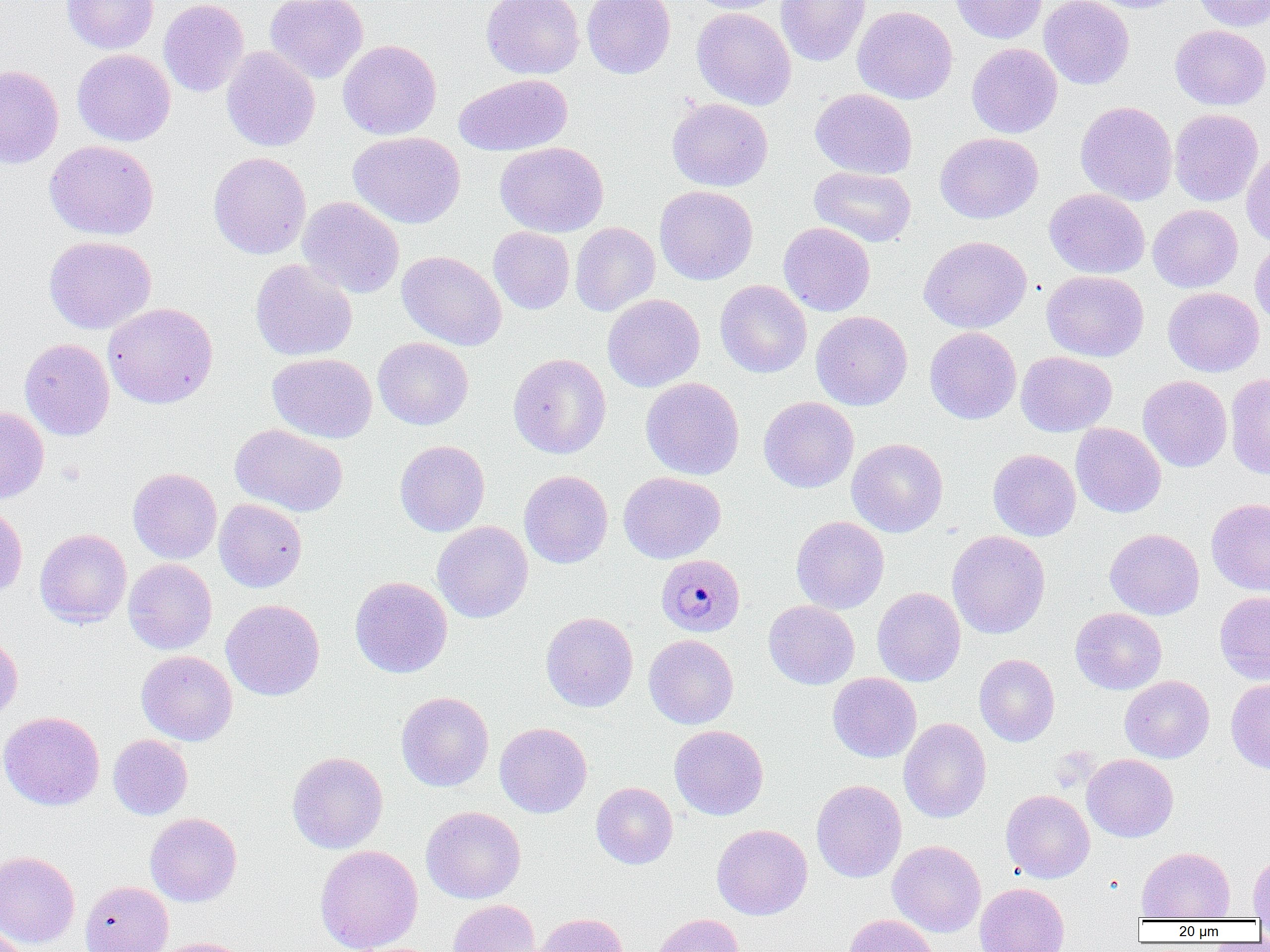
Summary:
  - Coordinate format: approximate bounding boxes as named x1/y1/x2/y2 corners in pixels
  - Plasmodium malariae-infected red blood cell locations: (x1=656, y1=553, x2=745, y2=637)
  - Uninfected red blood cell locations: (x1=61, y1=0, x2=159, y2=54), (x1=159, y1=0, x2=249, y2=97), (x1=265, y1=0, x2=368, y2=83), (x1=482, y1=0, x2=584, y2=79), (x1=582, y1=0, x2=676, y2=79), (x1=685, y1=0, x2=787, y2=14), (x1=776, y1=0, x2=871, y2=66), (x1=950, y1=0, x2=1047, y2=44), (x1=1039, y1=0, x2=1134, y2=89), (x1=1084, y1=0, x2=1187, y2=13), (x1=1191, y1=0, x2=1270, y2=32), (x1=852, y1=5, x2=958, y2=104), (x1=691, y1=7, x2=796, y2=110), (x1=1170, y1=25, x2=1270, y2=110), (x1=338, y1=39, x2=442, y2=140), (x1=966, y1=43, x2=1062, y2=138), (x1=221, y1=46, x2=320, y2=152), (x1=72, y1=49, x2=176, y2=147), (x1=0, y1=64, x2=64, y2=169), (x1=454, y1=73, x2=573, y2=156), (x1=810, y1=88, x2=918, y2=179), (x1=667, y1=97, x2=773, y2=191), (x1=1075, y1=101, x2=1177, y2=205), (x1=1169, y1=108, x2=1264, y2=206), (x1=348, y1=131, x2=466, y2=229), (x1=934, y1=132, x2=1043, y2=223), (x1=45, y1=140, x2=159, y2=240), (x1=496, y1=142, x2=609, y2=237), (x1=1241, y1=146, x2=1270, y2=246), (x1=208, y1=152, x2=312, y2=260), (x1=809, y1=165, x2=917, y2=247), (x1=654, y1=185, x2=758, y2=285), (x1=1044, y1=188, x2=1150, y2=278), (x1=297, y1=197, x2=405, y2=298), (x1=1148, y1=204, x2=1243, y2=293), (x1=570, y1=222, x2=660, y2=316), (x1=778, y1=222, x2=876, y2=316), (x1=488, y1=227, x2=575, y2=314), (x1=44, y1=235, x2=156, y2=334), (x1=918, y1=235, x2=1032, y2=333), (x1=1250, y1=240, x2=1270, y2=327), (x1=397, y1=250, x2=506, y2=350), (x1=250, y1=258, x2=358, y2=362), (x1=1042, y1=270, x2=1148, y2=361), (x1=715, y1=280, x2=812, y2=378), (x1=1163, y1=287, x2=1264, y2=377), (x1=602, y1=293, x2=705, y2=392), (x1=103, y1=302, x2=218, y2=409), (x1=811, y1=311, x2=912, y2=410), (x1=924, y1=326, x2=1022, y2=424), (x1=373, y1=337, x2=474, y2=430), (x1=19, y1=338, x2=115, y2=440), (x1=1016, y1=351, x2=1117, y2=436), (x1=267, y1=353, x2=377, y2=443), (x1=508, y1=353, x2=611, y2=458), (x1=1225, y1=373, x2=1270, y2=479), (x1=1138, y1=375, x2=1232, y2=472), (x1=640, y1=377, x2=744, y2=479), (x1=758, y1=396, x2=859, y2=493), (x1=0, y1=406, x2=49, y2=504), (x1=230, y1=423, x2=349, y2=517), (x1=1071, y1=423, x2=1166, y2=518), (x1=847, y1=438, x2=948, y2=537), (x1=395, y1=440, x2=490, y2=536), (x1=988, y1=449, x2=1081, y2=541), (x1=128, y1=468, x2=222, y2=564), (x1=519, y1=469, x2=613, y2=569), (x1=618, y1=471, x2=726, y2=563), (x1=214, y1=498, x2=307, y2=592), (x1=1206, y1=499, x2=1270, y2=596), (x1=0, y1=504, x2=27, y2=601), (x1=791, y1=516, x2=889, y2=614), (x1=432, y1=521, x2=533, y2=623), (x1=35, y1=528, x2=132, y2=628), (x1=1104, y1=528, x2=1204, y2=620), (x1=946, y1=531, x2=1050, y2=639), (x1=123, y1=559, x2=217, y2=654), (x1=350, y1=576, x2=453, y2=678), (x1=872, y1=587, x2=966, y2=686), (x1=1214, y1=591, x2=1270, y2=685), (x1=221, y1=599, x2=325, y2=701), (x1=763, y1=600, x2=860, y2=689), (x1=1070, y1=607, x2=1167, y2=694), (x1=540, y1=611, x2=638, y2=712), (x1=0, y1=633, x2=22, y2=726), (x1=644, y1=634, x2=739, y2=729), (x1=136, y1=650, x2=237, y2=745), (x1=974, y1=654, x2=1060, y2=746), (x1=827, y1=672, x2=921, y2=762), (x1=1119, y1=675, x2=1214, y2=763), (x1=1226, y1=678, x2=1270, y2=774), (x1=395, y1=691, x2=494, y2=791), (x1=0, y1=711, x2=104, y2=810), (x1=898, y1=718, x2=992, y2=823), (x1=495, y1=722, x2=592, y2=818), (x1=669, y1=725, x2=769, y2=820), (x1=107, y1=734, x2=193, y2=819), (x1=287, y1=751, x2=388, y2=853), (x1=1082, y1=754, x2=1178, y2=842), (x1=811, y1=779, x2=906, y2=883), (x1=591, y1=782, x2=678, y2=869), (x1=1001, y1=789, x2=1095, y2=883), (x1=421, y1=806, x2=526, y2=903), (x1=145, y1=813, x2=242, y2=906), (x1=712, y1=824, x2=812, y2=920), (x1=887, y1=840, x2=986, y2=937), (x1=314, y1=844, x2=423, y2=952), (x1=1137, y1=847, x2=1235, y2=920), (x1=0, y1=851, x2=80, y2=949), (x1=1248, y1=852, x2=1270, y2=919), (x1=80, y1=880, x2=173, y2=952), (x1=975, y1=882, x2=1070, y2=952), (x1=449, y1=899, x2=541, y2=952), (x1=534, y1=912, x2=630, y2=952), (x1=650, y1=913, x2=744, y2=952), (x1=844, y1=914, x2=939, y2=952), (x1=0, y1=926, x2=31, y2=952), (x1=152, y1=937, x2=254, y2=952)
  - Slide-level diagnosis: Plasmodium malariae
  - Image size: 1270×952 pixels
  - Modality: light microscopy
  - Field of view: single
  - Preparation: thin blood smear
  - Magnification: 1000x